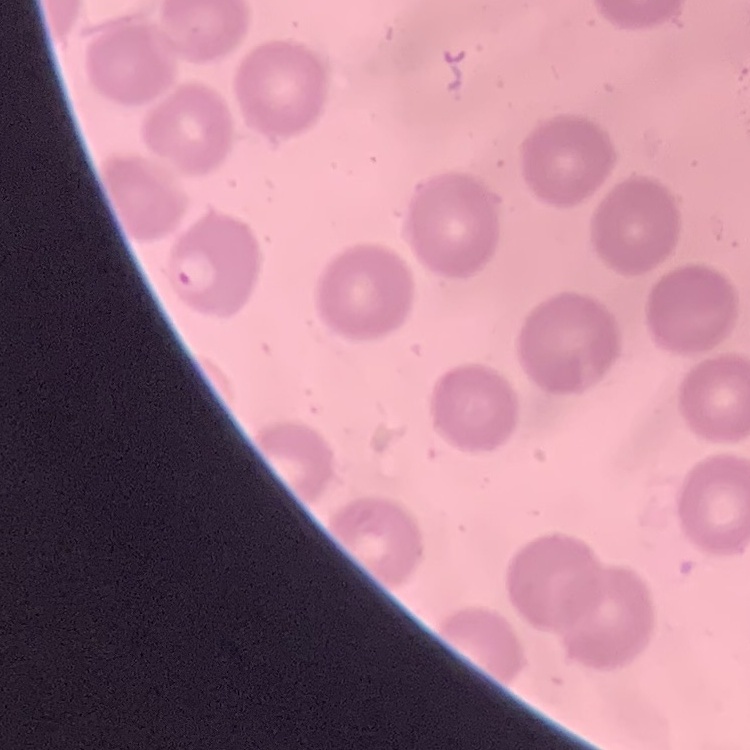

The erythrocytes show no rouleaux formation. Thin peripheral smear. One tile cut from a larger photomicrograph. Field's or Giemsa stain.